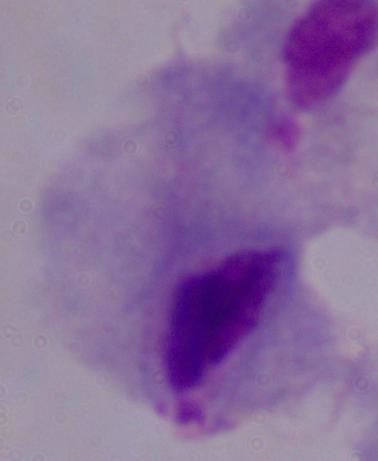

magnification: 1000x
identification: trichomonad
modality: micrograph